Give the extent of all Plasmodium vivax-infected red blood cells.
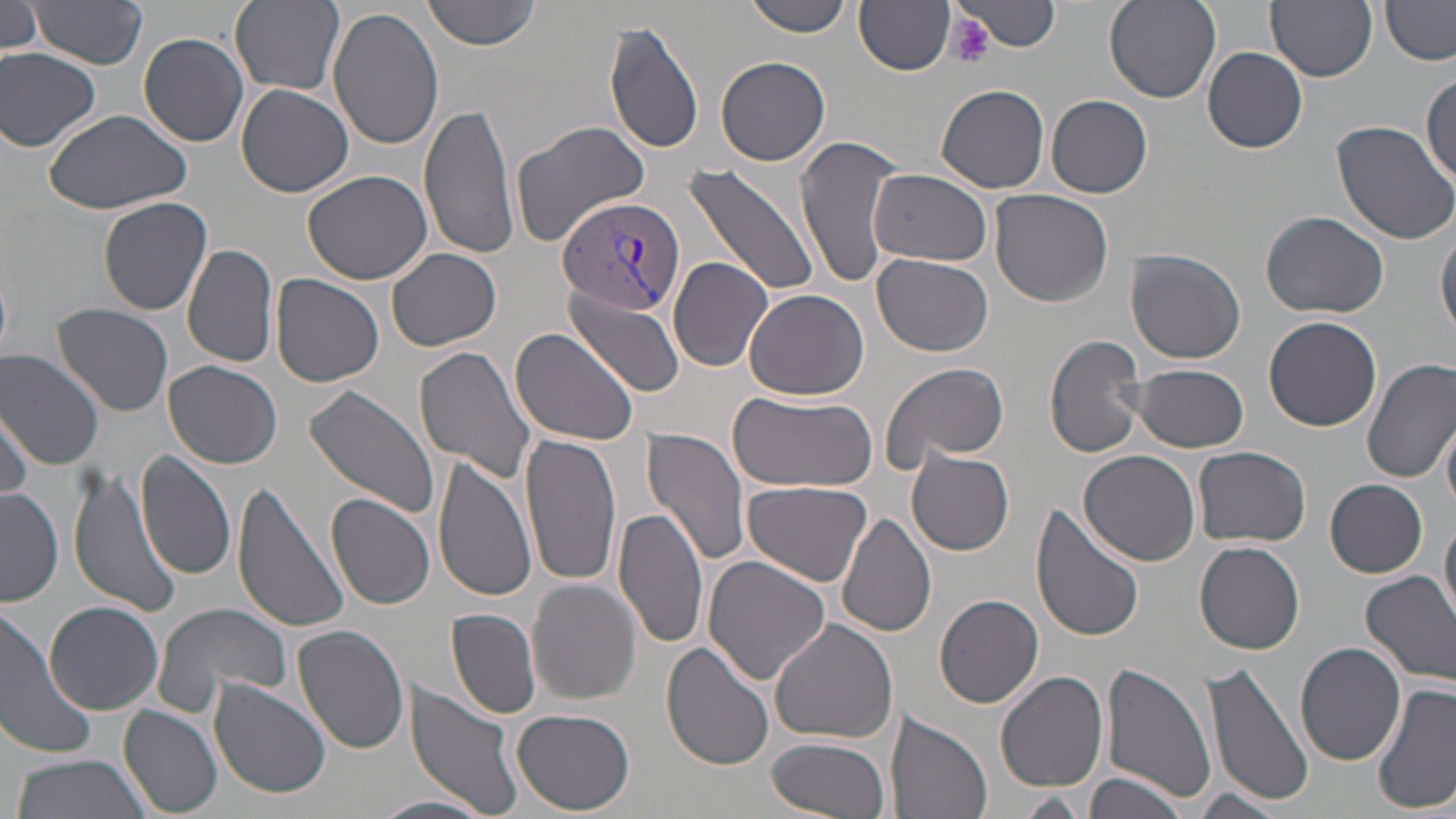
Approximate bounding boxes as (x1, y1, x2, y2) in pixels.
Plasmodium vivax-infected red blood cells: (557, 196, 684, 317).

Platelet locations: (946, 14, 997, 69). Uninfected red blood cell locations: (422, 0, 545, 50), (746, 0, 850, 37), (1267, 0, 1377, 82), (30, 1, 150, 67), (230, 1, 346, 94), (955, 1, 1060, 54), (1104, 1, 1219, 103), (1382, 1, 1456, 65), (856, 2, 956, 73), (1, 3, 47, 57), (328, 6, 446, 151), (603, 21, 708, 156), (139, 33, 250, 147), (1203, 46, 1307, 153), (0, 48, 101, 152), (715, 56, 831, 166), (1422, 76, 1456, 185), (938, 84, 1050, 194), (236, 85, 354, 199), (1046, 96, 1152, 198), (418, 100, 517, 258), (41, 106, 193, 214), (1330, 118, 1456, 246), (510, 120, 652, 247), (796, 135, 908, 291), (685, 161, 821, 296), (870, 168, 996, 267), (302, 170, 433, 285), (990, 190, 1114, 308), (97, 196, 214, 315), (1261, 212, 1388, 317), (1437, 225, 1456, 342), (182, 244, 279, 369), (386, 247, 502, 351), (1128, 249, 1246, 364), (871, 253, 994, 356), (668, 256, 772, 371), (271, 273, 384, 387), (562, 287, 686, 398), (744, 288, 869, 401), (52, 304, 174, 417), (1264, 316, 1382, 431), (510, 327, 640, 445), (1045, 333, 1151, 460), (414, 346, 539, 483), (0, 350, 106, 468), (1361, 358, 1456, 483), (163, 361, 283, 470), (878, 361, 1012, 474), (1130, 364, 1249, 453), (305, 384, 443, 521), (1, 385, 68, 494), (726, 390, 878, 492), (1, 404, 33, 505), (1440, 417, 1456, 516), (643, 427, 755, 568), (520, 432, 623, 588), (1192, 444, 1310, 547), (136, 449, 238, 582), (1081, 449, 1200, 564), (906, 450, 1015, 555), (431, 456, 536, 604), (68, 467, 185, 619), (741, 478, 874, 586), (1326, 479, 1429, 577), (234, 481, 353, 636), (1, 486, 61, 607), (327, 493, 436, 609), (1032, 502, 1146, 644), (613, 505, 708, 650), (1440, 513, 1456, 626), (837, 514, 936, 639), (1194, 540, 1304, 654), (704, 554, 832, 684), (1360, 570, 1456, 686), (526, 579, 642, 705), (934, 594, 1045, 708), (154, 600, 293, 714), (44, 602, 165, 714), (0, 608, 98, 761), (446, 608, 541, 719), (769, 617, 898, 743), (293, 625, 409, 755), (944, 625, 1089, 764), (1294, 642, 1407, 767), (662, 643, 775, 771), (1319, 652, 1456, 791), (1098, 661, 1216, 805), (1204, 661, 1313, 808), (993, 670, 1110, 792), (208, 678, 331, 798), (405, 682, 525, 818), (1372, 683, 1455, 813), (118, 703, 225, 816), (513, 709, 635, 815), (889, 711, 994, 819), (764, 738, 893, 819), (9, 753, 155, 819), (1085, 773, 1190, 819), (1191, 789, 1286, 817), (1010, 791, 1089, 816), (370, 795, 493, 819). Slide-level diagnosis: Plasmodium vivax. May-Grünwald-Giemsa stain. Light microscopy. Single field of view. 1000x magnification. Image is 1456×819 pixels. Thin blood film.